Identify the preparation type.
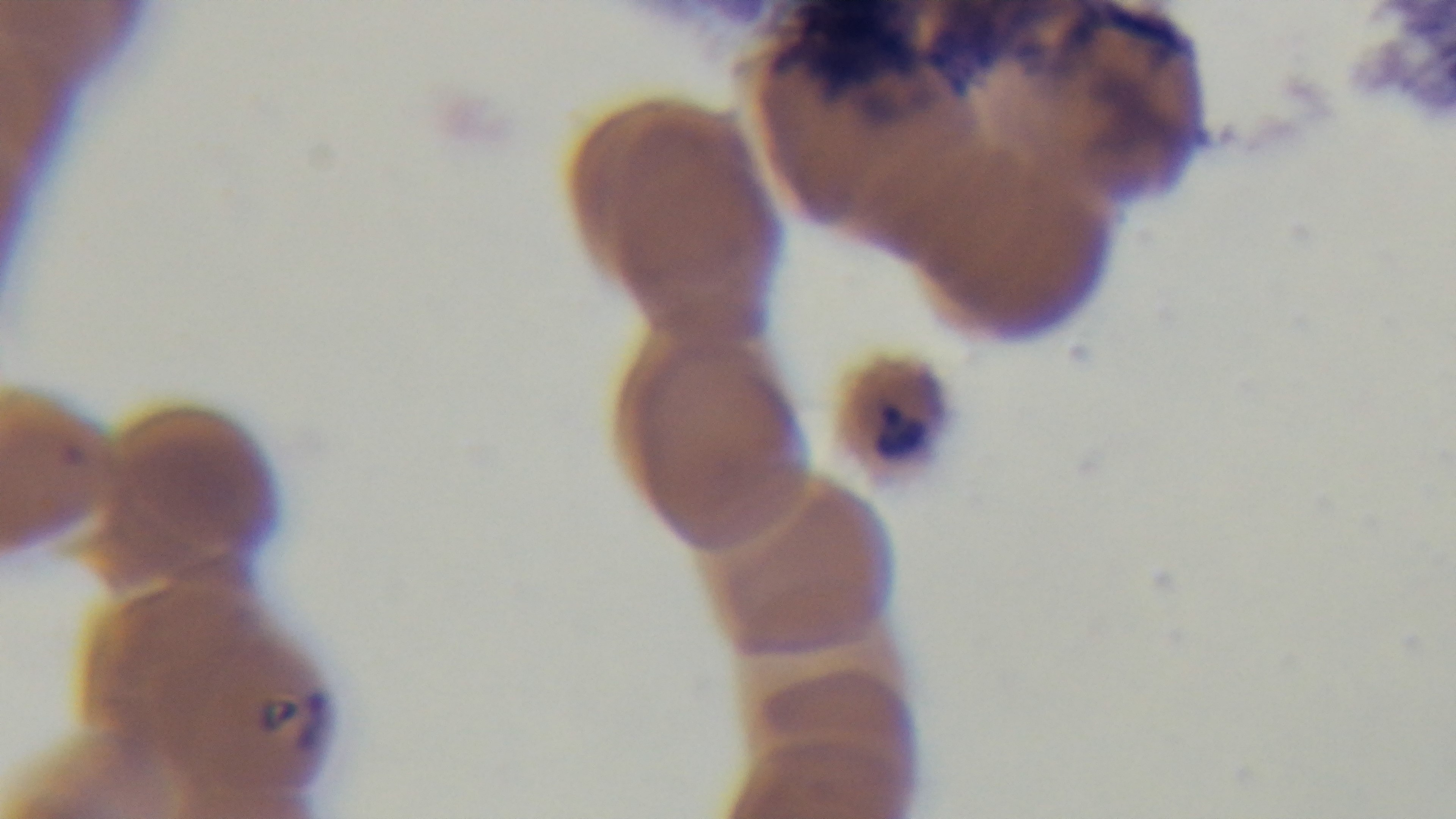

It is a thin blood film.

One field from the slide. Light microscopy. Malaria status: positive. Oil-immersion objective, 100x. Giemsa-stained. Mounted 4K digital camera.